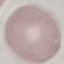 Result: no malaria parasites seen. Giemsa-stained preparation. Photographed with a smartphone camera at the microscope eyepiece. Thin smear of blood. Cell patch, automatically extracted from a larger field of view and resized to 64 × 64 pixels.